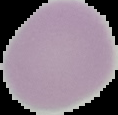

preparation = thin blood film
result = no malaria parasites detected
image size = 118×115 pixels
image type = cell region segmented out of the field of view; surrounding area masked to black